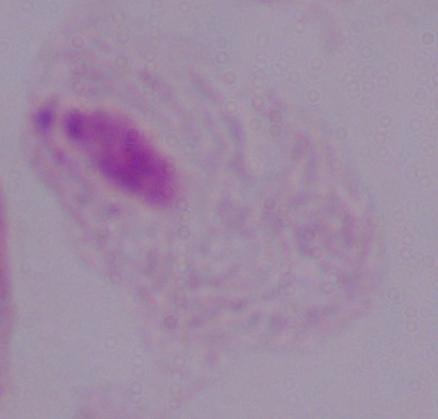
Summary:
  - Identification: trichomonad
  - Modality: photomicrograph
  - Magnification: 1000x